Name the cell type shown.
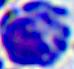

This is a leukocyte.

modality = micrograph
magnification = 400x